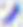

Captured at 400x magnification. Toxoplasma gondii is shown. Micrograph.